Comment on the morphology of the erythrocytes.
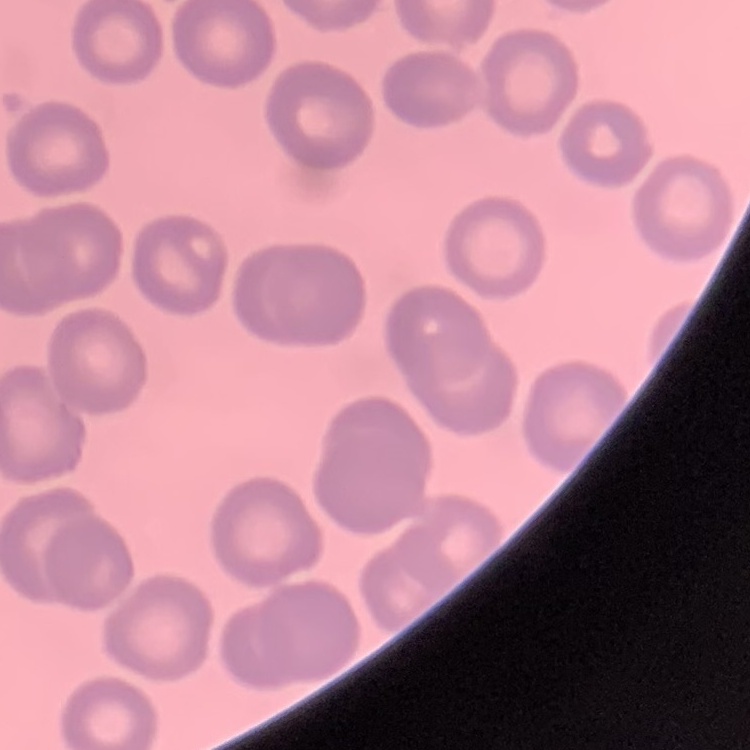

No rouleaux formation.

Summary:
  - Image type: square crop of a larger photomicrograph
  - Preparation: thin blood smear
  - Stain: Field's or Giemsa